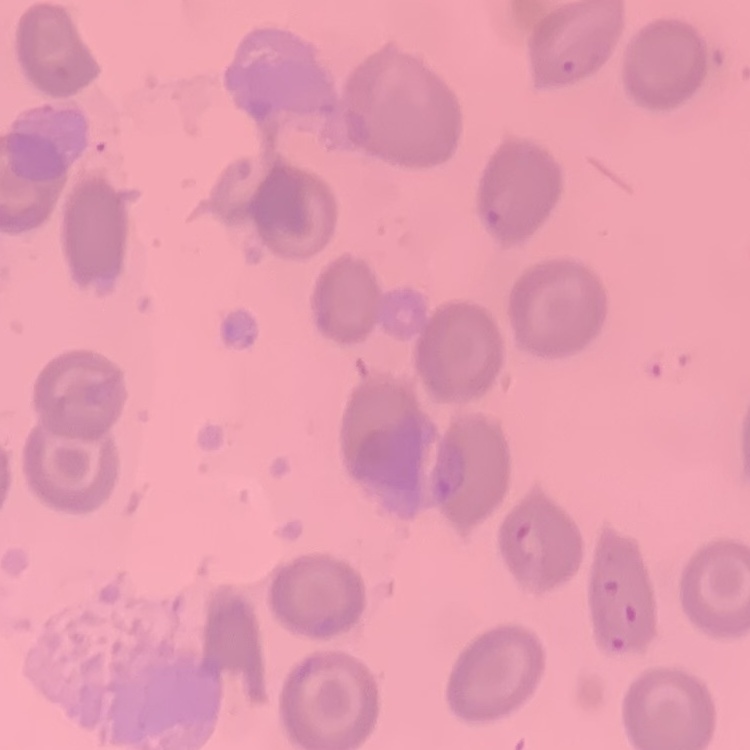

erythrocyte morphology = no rouleaux formation
image type = one tile cut from a larger photomicrograph
stain = Field's or Giemsa
preparation = thin peripheral smear